State the blood parasite species.
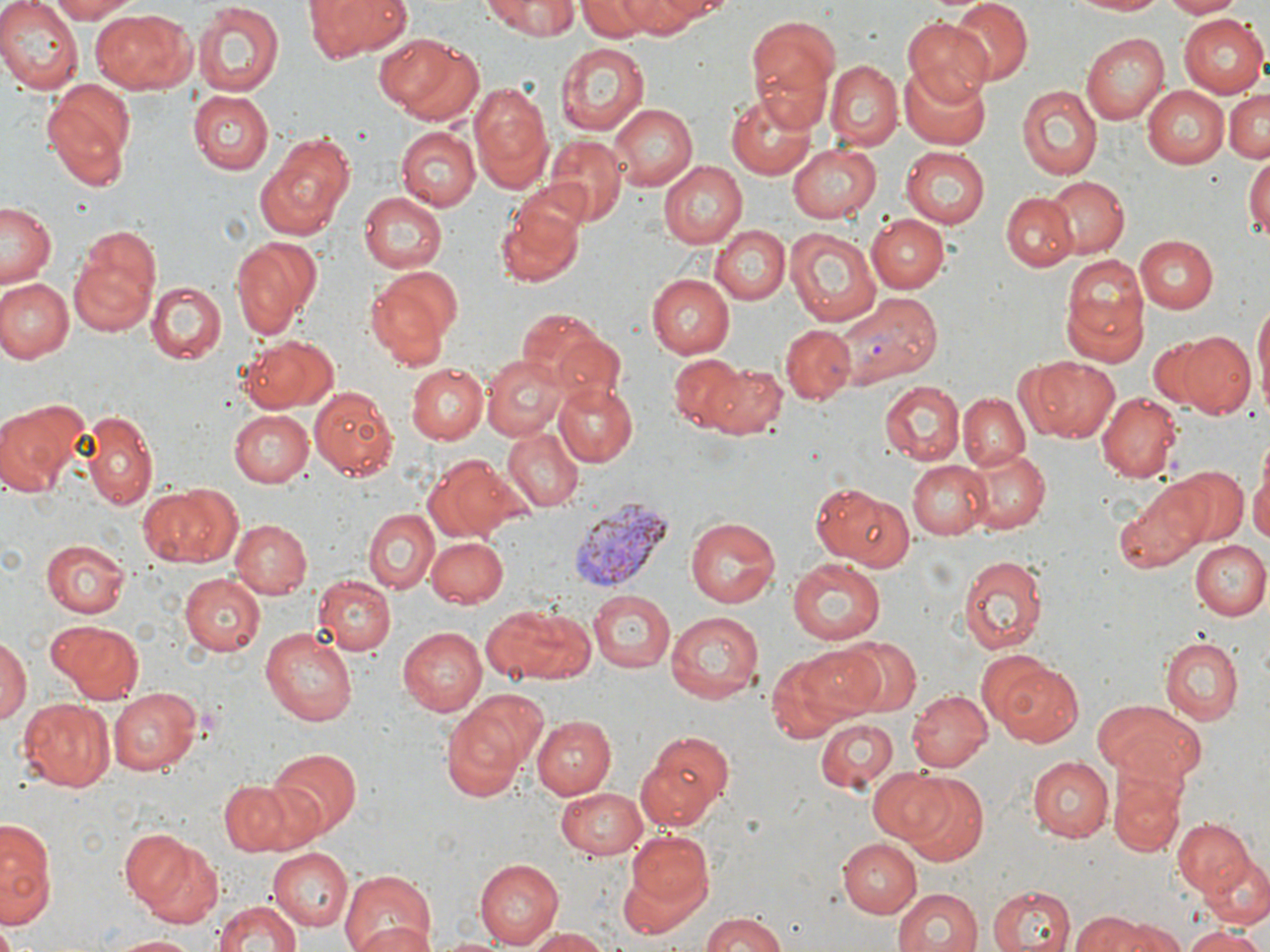

Plasmodium vivax.

Approximate bounding boxes as (x1,y1)-(x2,y2) corner pairs in pixels. Plasmodium vivax-infected red blood cell locations: (846,292)-(940,384), (568,497)-(673,593). Uninfected red blood cell locations: (0,0)-(82,93), (43,0)-(140,23), (309,0)-(410,60), (484,0)-(578,38), (579,0)-(666,40), (646,0)-(735,22), (947,0)-(1032,86), (1063,0)-(1173,17), (1160,0)-(1244,18), (613,1)-(702,38), (192,2)-(286,98), (91,8)-(200,93), (1181,12)-(1269,97), (743,14)-(843,129), (901,18)-(995,102), (1081,33)-(1167,124), (380,35)-(485,127), (554,41)-(648,135), (825,60)-(902,148), (900,62)-(992,148), (470,81)-(556,193), (1017,83)-(1102,178), (43,84)-(135,187), (1141,87)-(1228,170), (1223,88)-(1270,164), (187,91)-(273,175), (727,91)-(819,179), (610,103)-(698,191), (394,127)-(480,210), (257,133)-(353,239), (541,135)-(626,225), (786,142)-(881,222), (900,145)-(989,228), (1244,155)-(1270,242), (658,161)-(748,247), (1044,175)-(1129,257), (359,191)-(448,275), (493,192)-(587,289), (1000,192)-(1079,271), (1,201)-(58,289), (867,215)-(948,293), (712,226)-(789,304), (784,226)-(881,325), (71,227)-(161,331), (1136,234)-(1221,313), (229,235)-(323,339), (1060,255)-(1147,363), (363,270)-(459,368), (645,272)-(734,357), (1,278)-(73,362), (148,281)-(226,363), (1254,297)-(1269,414), (517,307)-(607,386), (781,323)-(855,402), (1176,331)-(1257,419), (242,334)-(339,414), (1144,335)-(1226,412), (552,336)-(629,412), (668,354)-(746,431), (482,355)-(569,439), (1013,358)-(1117,446), (703,361)-(786,439), (409,363)-(488,444), (882,378)-(967,463), (553,379)-(638,466), (307,385)-(398,481), (1095,393)-(1180,483), (958,394)-(1030,471), (0,398)-(86,498), (81,409)-(157,509), (230,410)-(313,487), (502,427)-(583,511), (960,447)-(1051,537), (1251,456)-(1270,556), (427,457)-(522,541), (907,460)-(990,540), (1172,466)-(1246,543), (811,480)-(914,570), (1113,480)-(1212,572), (137,483)-(238,567), (364,508)-(438,592), (684,515)-(781,609), (232,520)-(312,600), (426,538)-(507,608), (42,539)-(129,618), (1190,539)-(1269,619), (959,553)-(1047,656), (786,557)-(885,646), (181,571)-(268,655), (313,574)-(397,654), (588,589)-(675,672), (482,603)-(593,684), (665,609)-(767,705), (48,618)-(146,704), (260,626)-(360,728), (398,626)-(488,717), (0,635)-(30,723), (1160,636)-(1244,725), (838,637)-(922,718), (787,643)-(890,725), (768,653)-(853,742), (983,656)-(1085,746), (110,686)-(202,776), (907,688)-(990,773), (17,697)-(117,791), (1095,699)-(1204,785), (439,708)-(530,801), (533,715)-(617,799), (816,715)-(901,792), (639,730)-(734,830), (268,748)-(360,834), (1027,757)-(1114,842), (868,766)-(960,846), (1110,772)-(1187,858), (899,774)-(990,865), (221,783)-(290,854), (555,785)-(650,858), (0,816)-(56,927), (1172,818)-(1255,900), (118,829)-(197,910), (623,829)-(716,929), (1189,835)-(1269,929), (837,837)-(922,917), (134,838)-(226,930), (266,849)-(352,931), (474,858)-(561,947), (340,871)-(439,952), (987,885)-(1077,952), (892,887)-(982,952), (213,899)-(306,952), (700,910)-(791,952), (1069,912)-(1148,951), (1100,916)-(1182,952), (0,922)-(22,952), (352,922)-(432,952), (523,927)-(609,952), (1183,928)-(1268,952), (108,935)-(201,952). Thin blood smear. May-Grünwald-Giemsa-stained preparation. Single field of view. Image is 1270×952 pixels. Light microscopy. 1000x magnification.